Locate every blood parasite and identify its species.
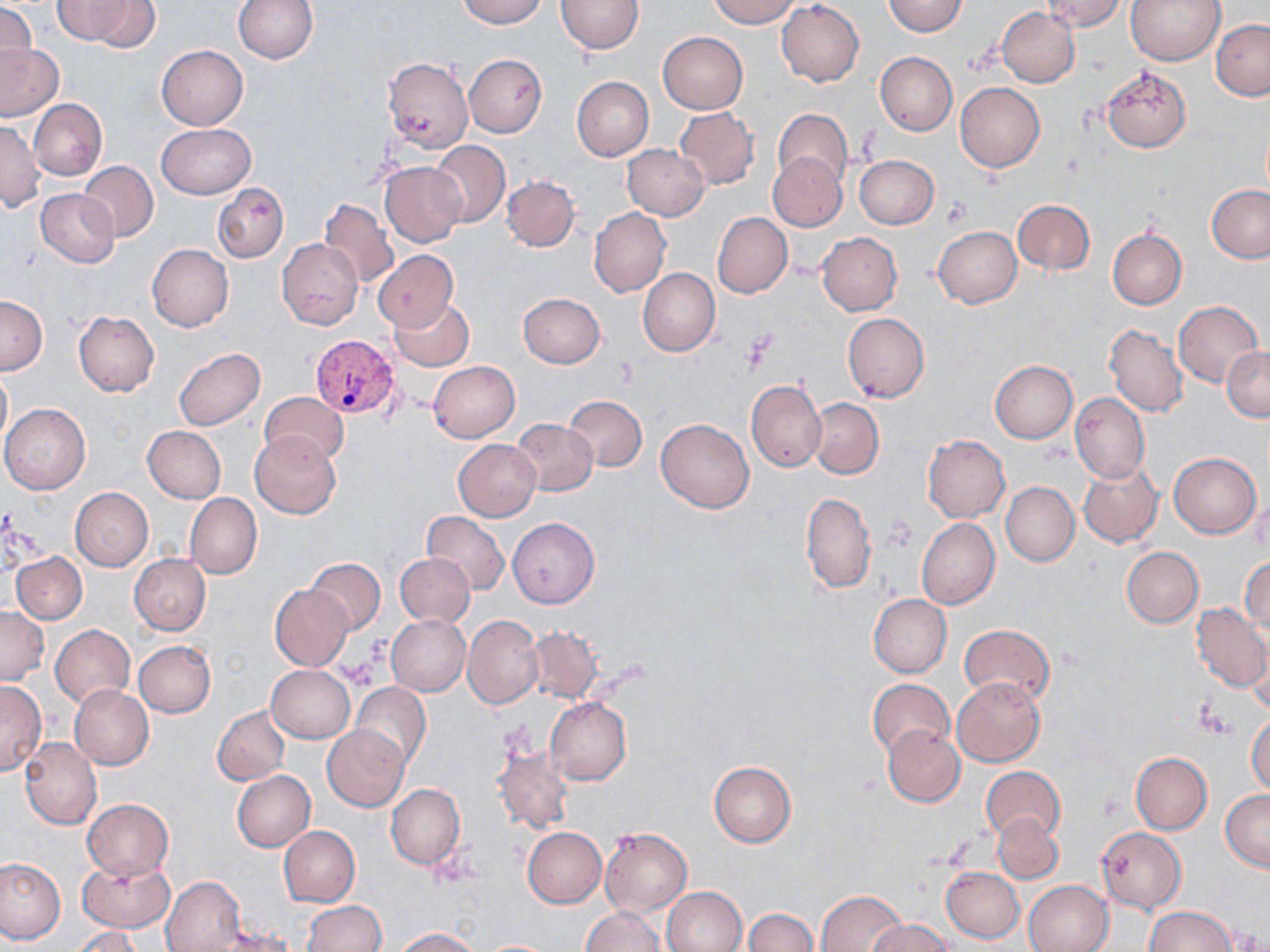

Approximate bounding boxes as named x1/y1/x2/y2 corners in pixels.
Plasmodium vivax-infected red blood cells: (x1=311, y1=333, x2=403, y2=417).
No Plasmodium falciparum, Plasmodium ovale, Plasmodium malariae, Babesia divergens, or Trypanosoma brucei observed.

Summary:
  - Platelet locations: (x1=941, y1=196, x2=972, y2=227), (x1=739, y1=331, x2=777, y2=372), (x1=337, y1=660, x2=379, y2=689), (x1=1195, y1=702, x2=1230, y2=739)
  - Uninfected red blood cell locations: (x1=69, y1=0, x2=159, y2=51), (x1=231, y1=0, x2=317, y2=64), (x1=457, y1=0, x2=546, y2=26), (x1=555, y1=0, x2=643, y2=54), (x1=706, y1=0, x2=801, y2=27), (x1=882, y1=0, x2=968, y2=36), (x1=1041, y1=0, x2=1129, y2=32), (x1=1125, y1=0, x2=1224, y2=65), (x1=777, y1=1, x2=864, y2=86), (x1=0, y1=3, x2=37, y2=79), (x1=996, y1=7, x2=1079, y2=88), (x1=1211, y1=19, x2=1270, y2=100), (x1=657, y1=32, x2=748, y2=114), (x1=0, y1=44, x2=63, y2=120), (x1=156, y1=45, x2=248, y2=130), (x1=875, y1=51, x2=957, y2=135), (x1=463, y1=54, x2=547, y2=137), (x1=384, y1=56, x2=473, y2=154), (x1=1102, y1=65, x2=1192, y2=153), (x1=572, y1=75, x2=654, y2=161), (x1=955, y1=83, x2=1045, y2=171), (x1=30, y1=99, x2=106, y2=179), (x1=674, y1=107, x2=760, y2=190), (x1=773, y1=108, x2=853, y2=190), (x1=0, y1=121, x2=43, y2=211), (x1=157, y1=122, x2=255, y2=198), (x1=428, y1=140, x2=510, y2=227), (x1=622, y1=145, x2=709, y2=221), (x1=768, y1=152, x2=846, y2=231), (x1=855, y1=154, x2=938, y2=228), (x1=78, y1=161, x2=159, y2=242), (x1=379, y1=161, x2=465, y2=248), (x1=502, y1=176, x2=579, y2=251), (x1=213, y1=185, x2=288, y2=262), (x1=1207, y1=185, x2=1270, y2=262), (x1=36, y1=188, x2=120, y2=269), (x1=319, y1=198, x2=400, y2=289), (x1=1012, y1=199, x2=1095, y2=275), (x1=589, y1=207, x2=670, y2=298), (x1=712, y1=212, x2=792, y2=298), (x1=933, y1=226, x2=1021, y2=308), (x1=1108, y1=227, x2=1187, y2=310), (x1=818, y1=233, x2=902, y2=315), (x1=277, y1=239, x2=362, y2=330), (x1=147, y1=243, x2=234, y2=332), (x1=374, y1=251, x2=458, y2=331), (x1=637, y1=268, x2=719, y2=356), (x1=519, y1=292, x2=605, y2=368), (x1=388, y1=296, x2=475, y2=372), (x1=0, y1=297, x2=47, y2=375), (x1=1173, y1=301, x2=1263, y2=388), (x1=74, y1=311, x2=159, y2=396), (x1=842, y1=313, x2=929, y2=403), (x1=1105, y1=324, x2=1189, y2=418), (x1=1223, y1=346, x2=1270, y2=420), (x1=173, y1=348, x2=265, y2=431), (x1=428, y1=361, x2=520, y2=442), (x1=990, y1=361, x2=1077, y2=443), (x1=0, y1=371, x2=11, y2=450), (x1=746, y1=380, x2=826, y2=473), (x1=259, y1=391, x2=349, y2=466), (x1=1070, y1=393, x2=1149, y2=483), (x1=565, y1=395, x2=646, y2=472), (x1=807, y1=398, x2=884, y2=478), (x1=1, y1=404, x2=90, y2=494), (x1=511, y1=418, x2=598, y2=496), (x1=656, y1=418, x2=754, y2=513), (x1=142, y1=426, x2=226, y2=503), (x1=249, y1=432, x2=341, y2=519), (x1=923, y1=435, x2=1009, y2=523), (x1=453, y1=439, x2=540, y2=520), (x1=1168, y1=452, x2=1261, y2=538), (x1=1079, y1=462, x2=1162, y2=547), (x1=1001, y1=482, x2=1080, y2=567), (x1=70, y1=488, x2=153, y2=571), (x1=801, y1=492, x2=876, y2=593), (x1=185, y1=493, x2=262, y2=579), (x1=422, y1=511, x2=509, y2=594), (x1=508, y1=518, x2=599, y2=608), (x1=917, y1=518, x2=999, y2=608), (x1=1121, y1=546, x2=1204, y2=627), (x1=13, y1=551, x2=87, y2=624), (x1=130, y1=553, x2=210, y2=635), (x1=394, y1=553, x2=475, y2=626), (x1=305, y1=557, x2=386, y2=634), (x1=1241, y1=557, x2=1269, y2=636), (x1=270, y1=585, x2=352, y2=669), (x1=869, y1=593, x2=951, y2=677), (x1=1192, y1=604, x2=1270, y2=691), (x1=0, y1=606, x2=48, y2=685), (x1=387, y1=615, x2=470, y2=696), (x1=462, y1=616, x2=542, y2=709), (x1=51, y1=625, x2=135, y2=709), (x1=959, y1=625, x2=1055, y2=705), (x1=524, y1=627, x2=603, y2=703), (x1=1248, y1=636, x2=1269, y2=717), (x1=134, y1=640, x2=216, y2=718), (x1=266, y1=664, x2=355, y2=743), (x1=866, y1=676, x2=953, y2=758), (x1=953, y1=677, x2=1045, y2=767), (x1=0, y1=679, x2=46, y2=776), (x1=350, y1=684, x2=431, y2=770), (x1=69, y1=685, x2=154, y2=769), (x1=546, y1=697, x2=631, y2=784), (x1=212, y1=706, x2=290, y2=785), (x1=1247, y1=712, x2=1270, y2=795), (x1=322, y1=724, x2=410, y2=811), (x1=881, y1=725, x2=965, y2=808), (x1=19, y1=737, x2=101, y2=829), (x1=493, y1=748, x2=574, y2=834), (x1=1130, y1=752, x2=1212, y2=834), (x1=708, y1=761, x2=796, y2=847), (x1=980, y1=766, x2=1066, y2=845), (x1=232, y1=770, x2=316, y2=851), (x1=386, y1=784, x2=465, y2=868), (x1=1221, y1=788, x2=1270, y2=871), (x1=83, y1=799, x2=172, y2=878), (x1=994, y1=812, x2=1062, y2=884), (x1=279, y1=826, x2=360, y2=907), (x1=522, y1=827, x2=607, y2=908), (x1=600, y1=827, x2=692, y2=917), (x1=1097, y1=827, x2=1186, y2=913), (x1=0, y1=857, x2=67, y2=946), (x1=76, y1=857, x2=175, y2=933), (x1=941, y1=866, x2=1024, y2=942), (x1=160, y1=875, x2=245, y2=952), (x1=1024, y1=880, x2=1113, y2=952), (x1=661, y1=886, x2=747, y2=952), (x1=815, y1=890, x2=908, y2=951), (x1=302, y1=901, x2=386, y2=952), (x1=1144, y1=906, x2=1236, y2=952), (x1=581, y1=907, x2=667, y2=952), (x1=743, y1=908, x2=818, y2=952), (x1=867, y1=918, x2=954, y2=951), (x1=72, y1=926, x2=143, y2=952), (x1=395, y1=928, x2=481, y2=951), (x1=483, y1=940, x2=555, y2=952)
  - Slide-level diagnosis: Plasmodium vivax
  - Magnification: 1000x
  - Field of view: single
  - Modality: light microscopy
  - Image size: 1270×952 pixels
  - Stain: May-Grünwald-Giemsa
  - Preparation: thin blood smear